Assess this cell for malaria.
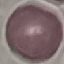

It is uninfected.

Acquired by smartphone through the microscope eyepiece. Thin smear of blood. Giemsa stain. Cell patch, automatically extracted from a larger field of view and resized to 64 × 64 pixels.